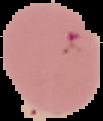
preparation = thin blood smear
result = Plasmodium parasites identified
image size = 103×121 pixels
image type = segmented cell region with the area outside set to black